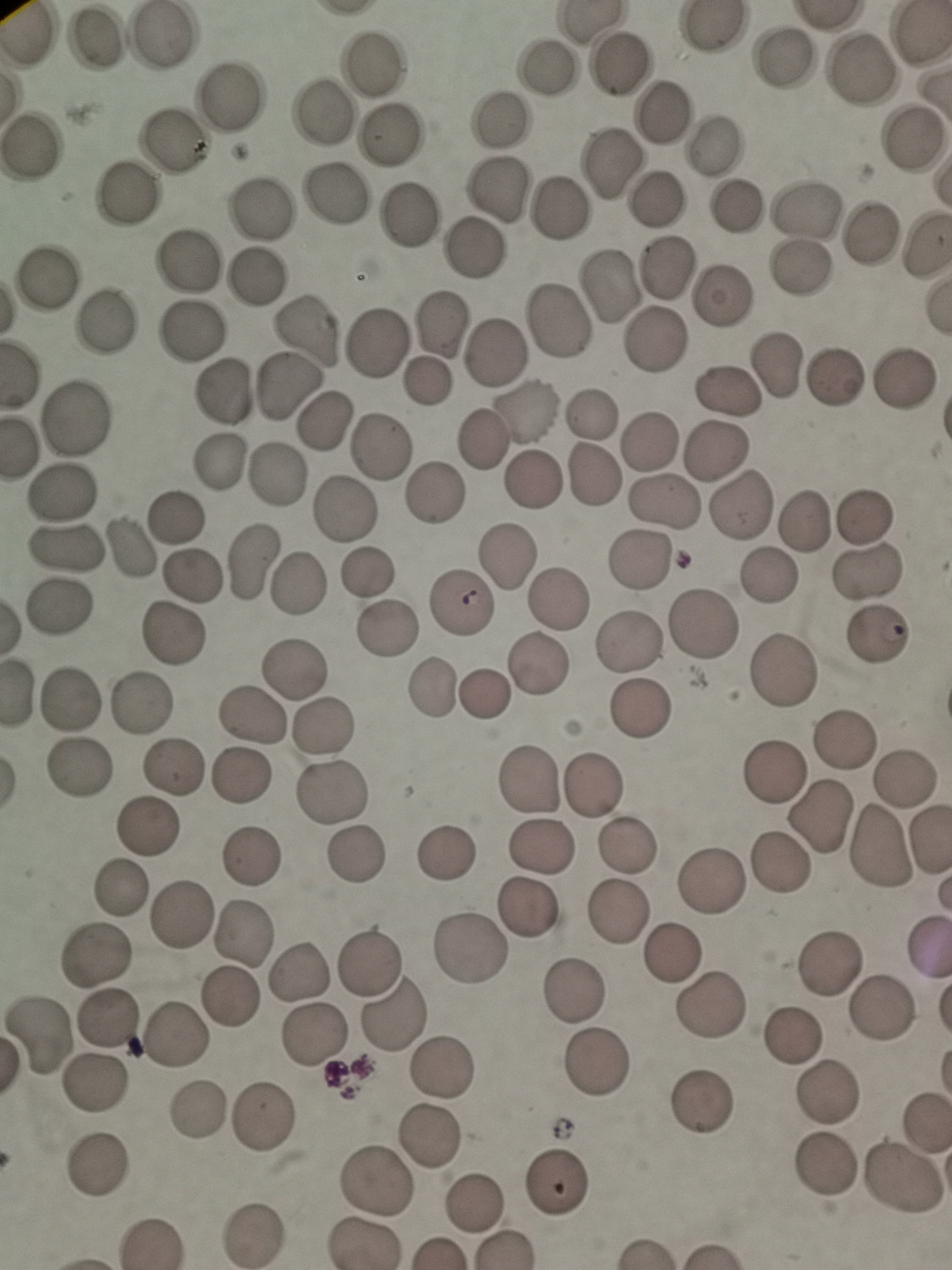
Approximate centers as (x, y) in pixels.
Summary:
  - Cell locations: (709, 26), (93, 38), (162, 38), (784, 56), (371, 62), (546, 67), (617, 67), (861, 69), (230, 95), (320, 113), (662, 115), (501, 121), (388, 135), (910, 140), (174, 142), (713, 148), (31, 149), (610, 165), (497, 190), (128, 191), (334, 195), (657, 202), (738, 208), (259, 209), (560, 209), (804, 209), (410, 213), (869, 234), (475, 248), (188, 262), (668, 266), (801, 267), (255, 277), (46, 279), (610, 288), (722, 299), (104, 320), (559, 321), (440, 323), (188, 330), (307, 333), (655, 341), (377, 344), (496, 351), (778, 363), (838, 374), (905, 380), (427, 383), (288, 385), (727, 389), (224, 391), (528, 411), (592, 412), (75, 418), (325, 421), (479, 439), (651, 443), (382, 447), (720, 450), (220, 461), (277, 474), (533, 479), (591, 480), (436, 492), (60, 493), (664, 500), (744, 504), (345, 510), (866, 514), (173, 516), (807, 520), (64, 549), (132, 551), (508, 559), (640, 559), (254, 562), (367, 572), (868, 573), (195, 577), (768, 577), (296, 585), (558, 600), (459, 604), (59, 607), (705, 626), (390, 628), (176, 634), (874, 641), (631, 645), (539, 662), (293, 669), (784, 671), (430, 689), (485, 693), (71, 700), (142, 704), (642, 710), (249, 715), (321, 726), (842, 739), (174, 767), (86, 769), (777, 771), (243, 775), (905, 779), (527, 782), (593, 786), (334, 794), (821, 817), (149, 827), (930, 840), (627, 843), (541, 846), (879, 851), (447, 855), (355, 856), (252, 857), (780, 867), (713, 882), (123, 890), (530, 908), (179, 913), (617, 916), (244, 933), (926, 948), (472, 949), (673, 953), (98, 955), (371, 959), (829, 966), (299, 973), (573, 992), (230, 1001), (708, 1009), (392, 1010), (882, 1010), (107, 1018), (317, 1034), (791, 1035), (40, 1036), (174, 1036), (599, 1065), (443, 1066), (94, 1084), (828, 1095), (703, 1105), (199, 1112), (264, 1118), (926, 1121), (431, 1134), (825, 1165), (96, 1166), (904, 1179), (555, 1180), (375, 1183), (475, 1206), (255, 1234), (359, 1243)
  - Field of view: single
  - Preparation: thin smear
  - Image size: 952×1270 pixels
  - Stain: Giemsa
  - Capture: smartphone through the microscope eyepiece